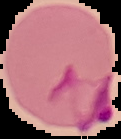
Image is 121×139 pixels. From a thin blood smear. Result: malaria parasites detected. Cell region segmented out of the field of view; the surrounding area is masked to black.